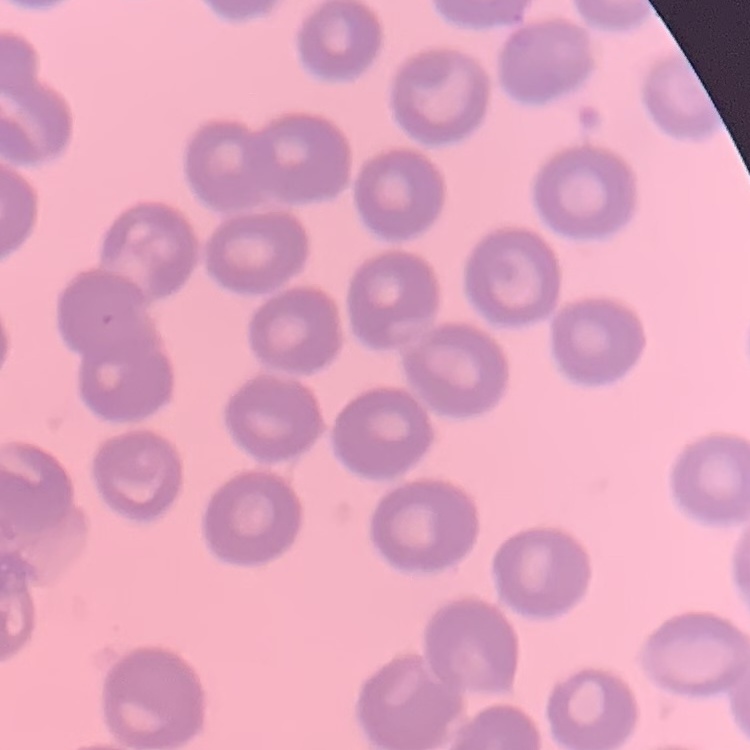 The erythrocytes show no rouleaux formation. Field's or Giemsa stain. Thin blood smear. One tile cut from a larger photomicrograph.